Describe the morphology of the erythrocytes.
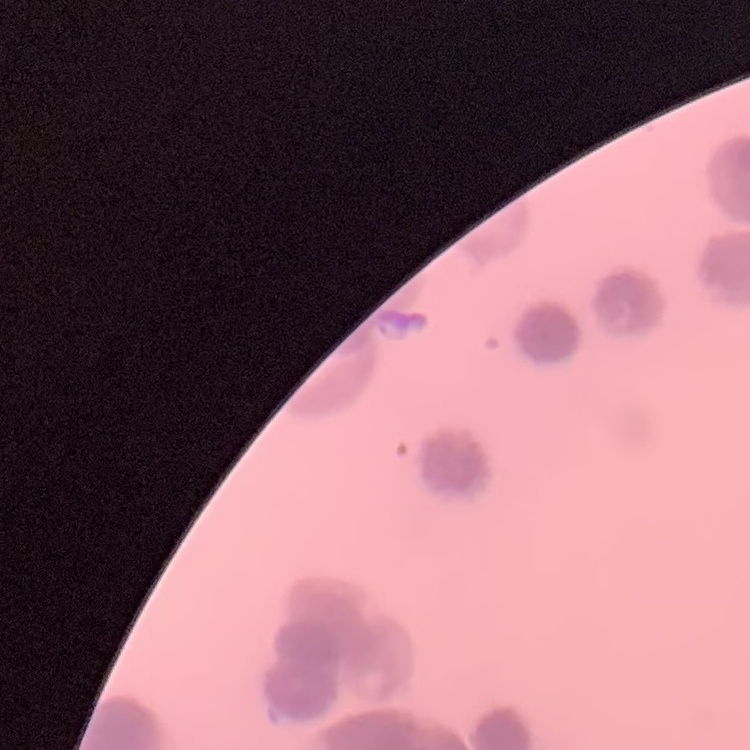

Rouleaux formation.

stain: Field's or Giemsa
image_type: one tile cut from a larger photomicrograph
preparation: thin peripheral smear